Give the extent of all Plasmodium ovale-infected red blood cells.
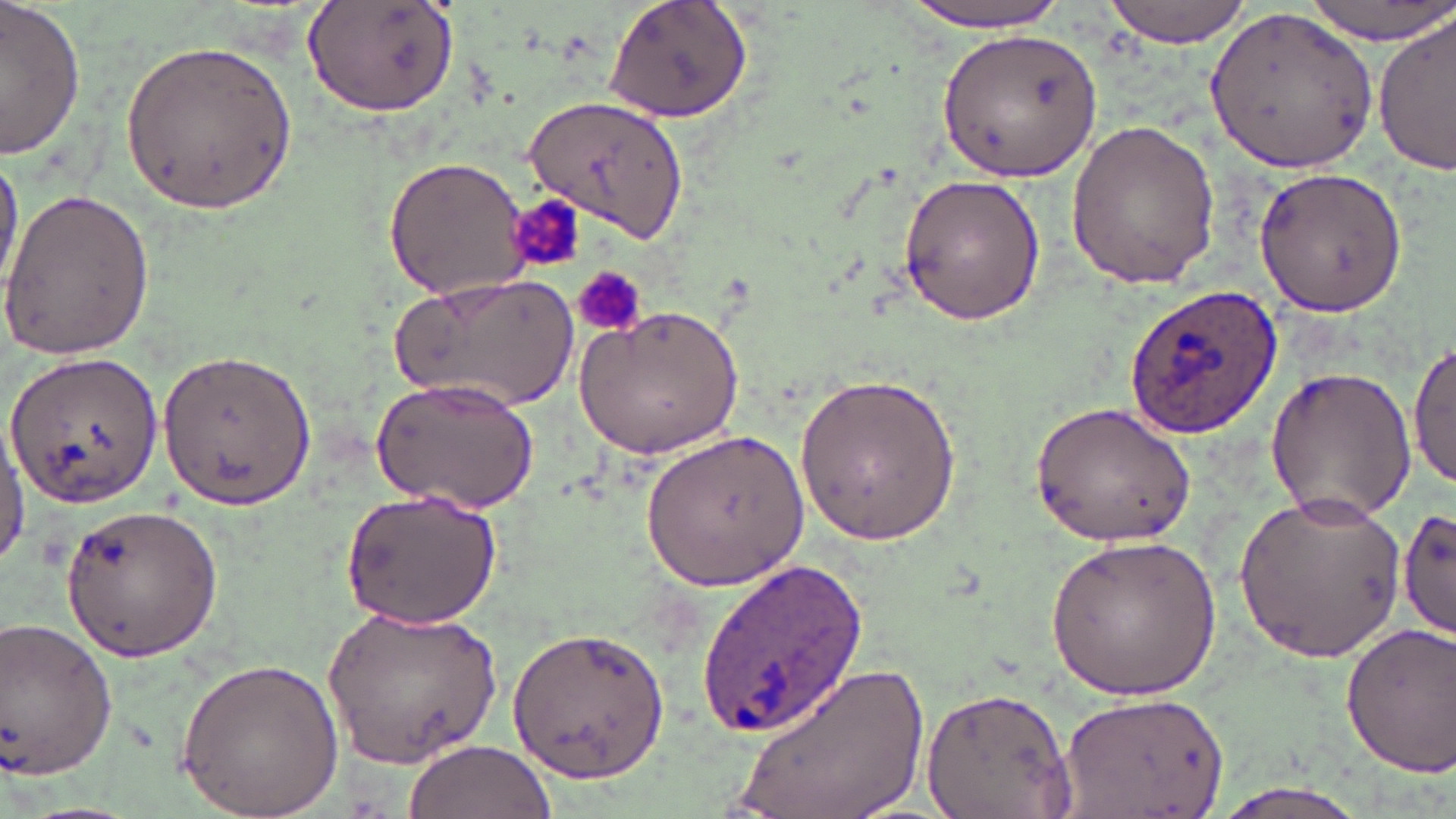
Approximate bounding boxes as named x1/y1/x2/y2 corners in pixels.
Plasmodium ovale-infected red blood cells: (x1=1124, y1=284, x2=1283, y2=439).

Summary:
  - Uninfected red blood cell locations: (x1=602, y1=0, x2=755, y2=123), (x1=1101, y1=0, x2=1251, y2=45), (x1=1300, y1=0, x2=1451, y2=42), (x1=896, y1=1, x2=1075, y2=32), (x1=1, y1=2, x2=85, y2=161), (x1=301, y1=2, x2=460, y2=116), (x1=1211, y1=3, x2=1382, y2=170), (x1=1374, y1=14, x2=1454, y2=175), (x1=937, y1=27, x2=1102, y2=184), (x1=120, y1=37, x2=296, y2=216), (x1=524, y1=95, x2=692, y2=246), (x1=1063, y1=116, x2=1220, y2=290), (x1=0, y1=148, x2=23, y2=296), (x1=382, y1=156, x2=533, y2=301), (x1=1255, y1=165, x2=1409, y2=315), (x1=896, y1=174, x2=1045, y2=326), (x1=0, y1=185, x2=154, y2=361), (x1=391, y1=271, x2=578, y2=412), (x1=573, y1=304, x2=743, y2=460), (x1=1411, y1=339, x2=1456, y2=493), (x1=155, y1=345, x2=315, y2=511), (x1=4, y1=348, x2=166, y2=509), (x1=1261, y1=364, x2=1418, y2=523), (x1=795, y1=369, x2=962, y2=549), (x1=371, y1=376, x2=540, y2=512), (x1=1026, y1=399, x2=1199, y2=550), (x1=0, y1=417, x2=29, y2=566), (x1=642, y1=428, x2=811, y2=590), (x1=340, y1=490, x2=503, y2=628), (x1=1230, y1=490, x2=1408, y2=664), (x1=56, y1=500, x2=228, y2=664), (x1=1395, y1=507, x2=1455, y2=642), (x1=1045, y1=530, x2=1222, y2=701), (x1=694, y1=556, x2=869, y2=736), (x1=325, y1=604, x2=503, y2=767), (x1=0, y1=614, x2=119, y2=784), (x1=1339, y1=622, x2=1456, y2=776), (x1=508, y1=623, x2=671, y2=783), (x1=176, y1=654, x2=344, y2=817), (x1=737, y1=658, x2=931, y2=818), (x1=919, y1=686, x2=1080, y2=819), (x1=1058, y1=689, x2=1228, y2=819), (x1=401, y1=739, x2=555, y2=819), (x1=1203, y1=779, x2=1381, y2=819)
  - Platelet locations: (x1=504, y1=201, x2=586, y2=282), (x1=572, y1=266, x2=648, y2=336)
  - Slide-level diagnosis: Plasmodium ovale
  - Magnification: 1000x
  - Preparation: thin blood smear
  - Field of view: one of a larger specimen
  - Stain: May-Grünwald-Giemsa
  - Modality: light microscopy
  - Image size: 1456×819 pixels